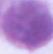

modality = micrograph
identification = erythrocyte
magnification = 1000x